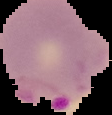

Summary:
  - Preparation: thin blood film
  - Image type: segmented cell region on a black background
  - Malaria status: parasitized
  - Image size: 112×115 pixels